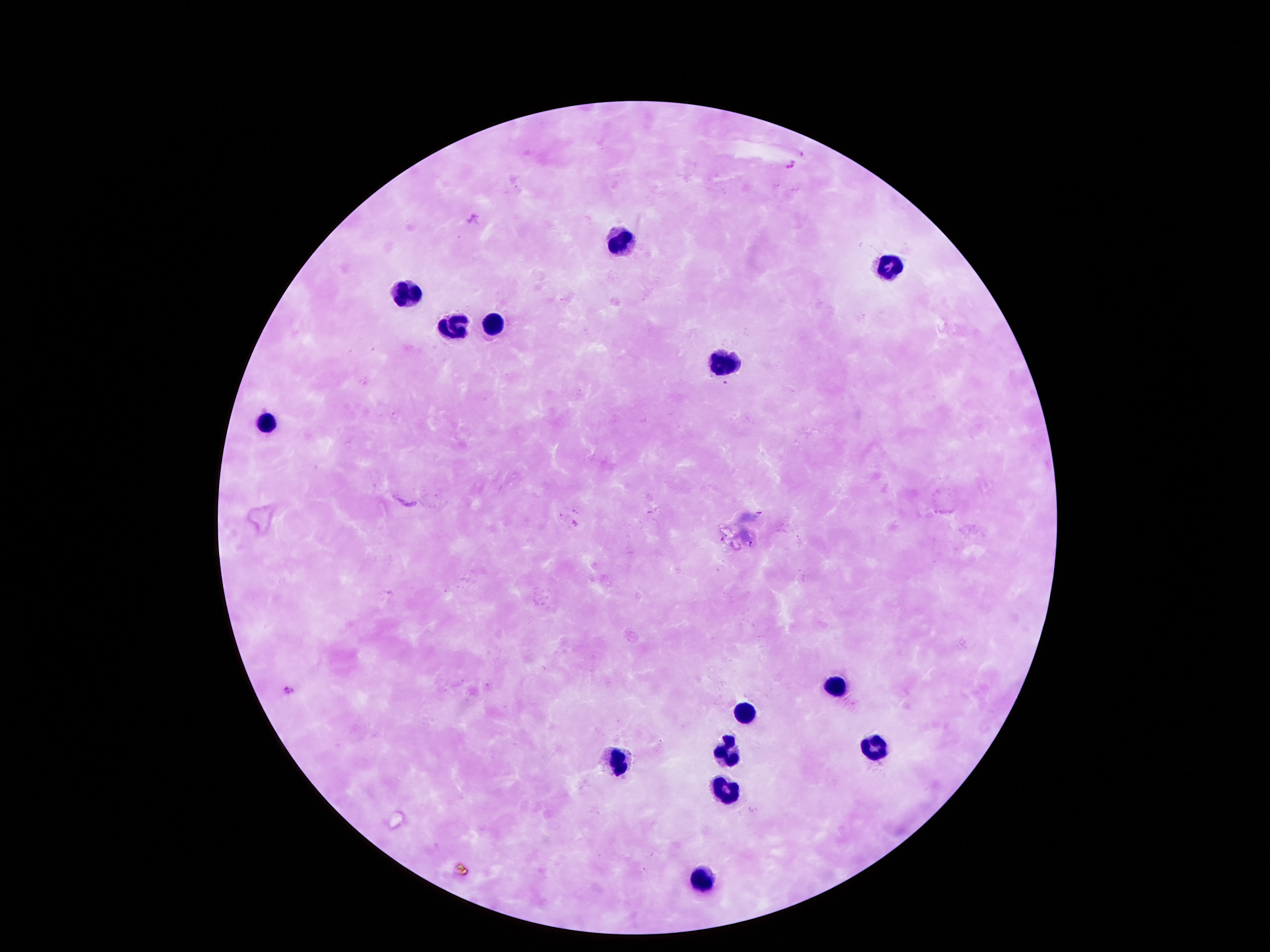
Approximate centers as {x, y} in pixels.
Summary:
  - Leukocyte locations: {612, 245}, {891, 264}, {407, 291}, {494, 319}, {454, 323}, {723, 363}, {269, 419}, {834, 685}, {743, 711}, {874, 746}, {723, 748}, {615, 763}, {726, 788}, {699, 880}
  - Capture: smartphone camera through the microscope eyepiece
  - Preparation: thick blood film
  - Stain: Giemsa
  - Field of view: single
  - Magnification: 100x
  - Patient malaria status: not infected
  - Image size: 1270×952 pixels